Assess the morphology of the erythrocytes.
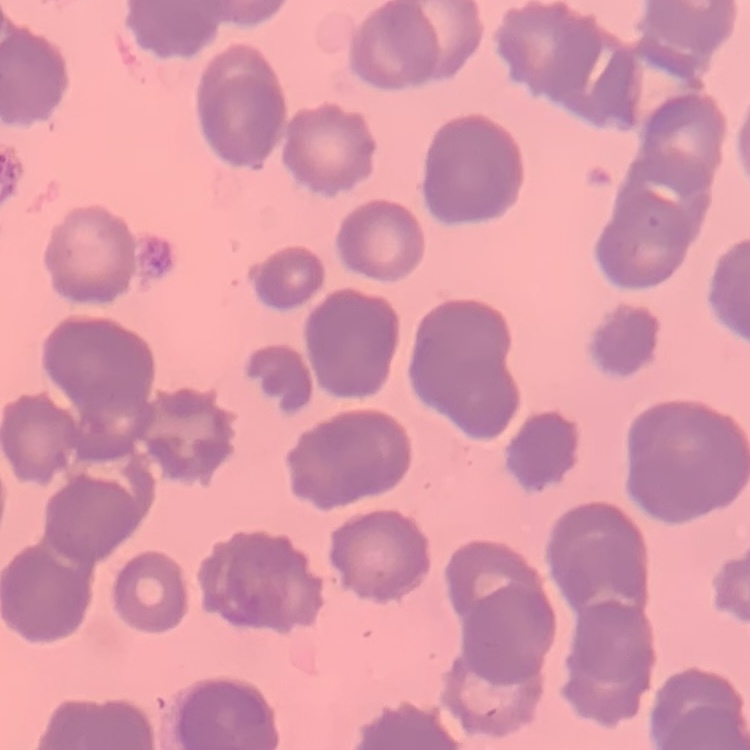
Rouleaux formation.

Summary:
  - Image type: square crop of a larger photomicrograph
  - Stain: Field's or Giemsa
  - Preparation: thin blood smear